State which parasite is depicted.
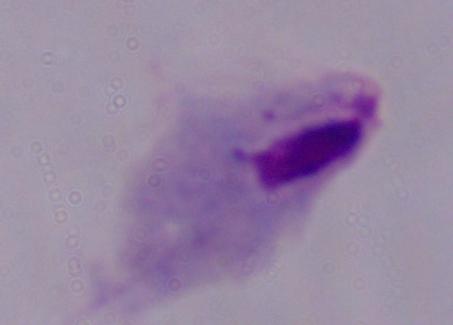
This is a trichomonad.

1000x magnification. Photomicrograph.